Locate and identify every blood parasite.
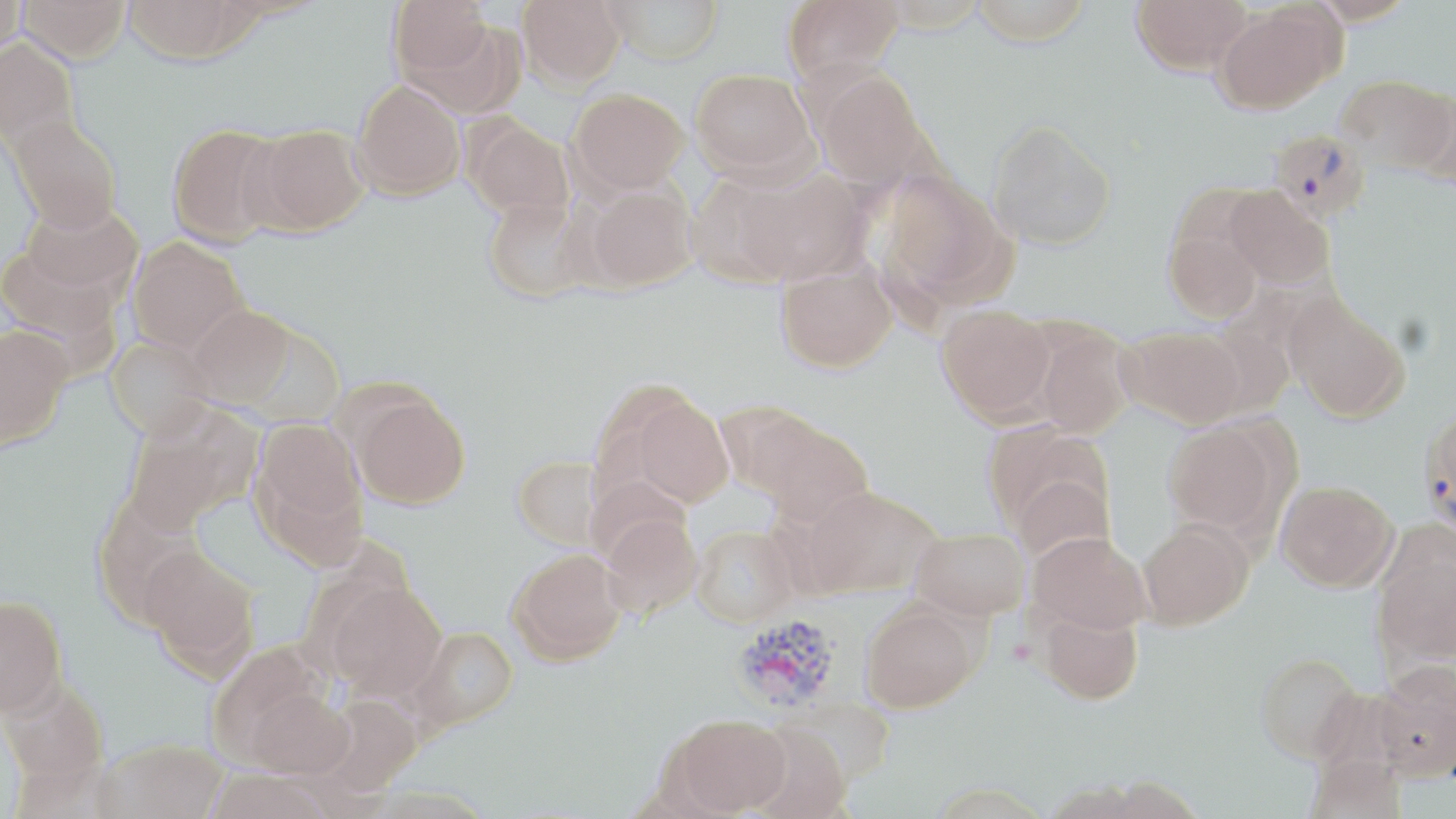

Approximate bounding boxes as (x1,y1)-(x2,y2) corner pairs in pixels.
Plasmodium vivax-infected red blood cells: (1267,128)-(1370,221), (1419,409)-(1456,536), (731,613)-(844,715).
No Plasmodium falciparum, Plasmodium ovale, Plasmodium malariae, Babesia divergens, or Trypanosoma brucei observed.

Uninfected red blood cell locations: (0,0)-(28,57), (17,0)-(128,66), (121,0)-(259,69), (389,0)-(494,88), (517,0)-(626,88), (604,0)-(725,64), (782,0)-(904,84), (969,0)-(1095,45), (1131,0)-(1252,75), (1309,0)-(1417,25), (1213,4)-(1341,114), (0,41)-(78,150), (691,67)-(816,178), (817,72)-(933,190), (1337,74)-(1456,174), (353,81)-(465,199), (570,88)-(689,195), (1412,88)-(1456,187), (8,117)-(122,238), (465,118)-(574,223), (986,118)-(1117,251), (167,124)-(288,248), (248,126)-(368,235), (723,166)-(869,286), (880,170)-(1006,301), (587,183)-(698,289), (1225,187)-(1334,289), (483,196)-(593,302), (22,204)-(143,300), (1165,223)-(1263,322), (128,239)-(249,357), (0,247)-(121,347), (776,262)-(896,373), (1284,294)-(1409,423), (937,304)-(1056,423), (188,307)-(296,410), (1034,326)-(1132,439), (1121,326)-(1245,429), (0,329)-(73,453), (105,340)-(217,445), (350,392)-(469,509), (631,396)-(733,507), (122,413)-(250,535), (753,417)-(874,525), (253,419)-(365,541), (1161,420)-(1287,538), (988,424)-(1117,546), (512,455)-(606,549), (1009,475)-(1115,564), (1276,479)-(1398,591), (804,486)-(939,597), (601,513)-(704,617), (1139,518)-(1253,629), (692,525)-(799,627), (911,527)-(1030,619), (1028,531)-(1151,635), (1373,532)-(1456,665), (141,548)-(259,677), (509,548)-(626,664), (326,582)-(445,700), (0,599)-(67,721), (861,602)-(978,712), (1039,607)-(1143,704), (410,626)-(519,731), (1254,651)-(1364,764), (1373,662)-(1456,781), (1,683)-(109,792), (242,687)-(355,779), (315,694)-(424,798), (671,714)-(790,816), (748,723)-(850,819), (97,741)-(227,819), (202,771)-(333,819). Slide-level diagnosis: Plasmodium vivax. Thin blood film. May-Grünwald-Giemsa-stained preparation. Single field of view. Optical microscopy. 1000x magnification. Image is 1456×819 pixels.